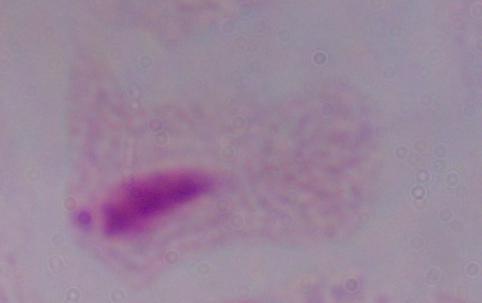
magnification = 1000x
modality = micrograph
identification = trichomonad